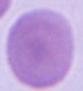

{
  "magnification": "1000x",
  "identification": "red blood cell",
  "modality": "photomicrograph"
}